State which parasite is depicted.
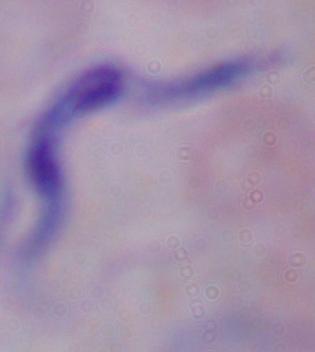

A trypanosome.

magnification = 1000x
modality = photomicrograph